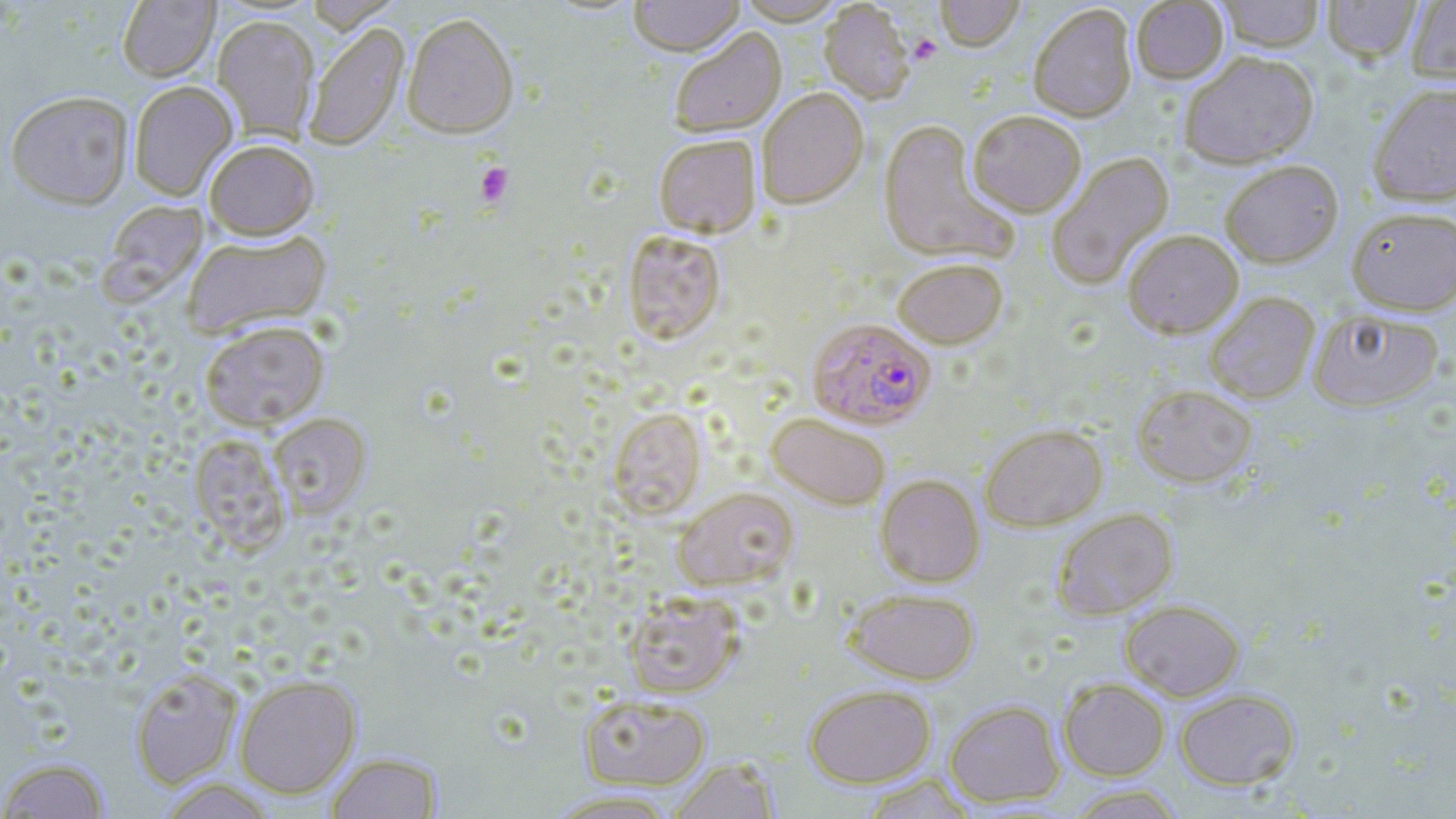 Approximate bounding boxes as [x1, y1, x2, y2] in pixels. Uninfected red blood cell locations: [303, 0, 401, 32], [629, 0, 744, 56], [736, 0, 847, 24], [936, 0, 1024, 51], [1215, 0, 1326, 51], [1322, 0, 1422, 64], [1406, 0, 1456, 84], [117, 1, 219, 82], [818, 1, 915, 103], [1131, 1, 1228, 83], [1028, 3, 1138, 122], [402, 12, 519, 139], [212, 14, 320, 141], [303, 21, 410, 152], [668, 27, 786, 137], [1179, 50, 1318, 168], [128, 80, 238, 201], [1368, 81, 1456, 206], [756, 87, 869, 208], [6, 89, 133, 209], [968, 110, 1086, 216], [877, 121, 1016, 265], [653, 134, 761, 238], [204, 139, 320, 239], [1046, 151, 1174, 290], [1219, 159, 1344, 268], [97, 200, 208, 305], [1345, 205, 1456, 315], [621, 229, 726, 345], [1122, 229, 1244, 337], [182, 230, 333, 338], [892, 257, 1008, 348], [1204, 292, 1320, 404], [1307, 307, 1445, 412], [199, 320, 330, 430], [1132, 384, 1258, 488], [607, 407, 706, 520], [765, 411, 892, 510], [267, 413, 371, 519], [980, 423, 1108, 530], [189, 434, 291, 553], [875, 474, 985, 587], [672, 486, 798, 590], [1050, 507, 1178, 620], [846, 587, 979, 685], [622, 590, 745, 698], [1119, 598, 1245, 701], [130, 668, 242, 789], [234, 674, 361, 798], [1058, 677, 1170, 781], [804, 683, 936, 788], [1174, 688, 1300, 790], [579, 693, 711, 790], [944, 699, 1065, 807], [324, 752, 444, 818], [0, 757, 112, 818], [668, 758, 781, 818], [860, 774, 978, 818], [155, 778, 279, 819], [1064, 784, 1187, 818], [542, 789, 682, 818]. Plasmodium falciparum-infected red blood cell locations: [807, 317, 936, 429]. Platelet locations: [908, 35, 941, 65], [475, 163, 514, 207]. Slide-level diagnosis: Plasmodium falciparum. One field of a larger specimen. Image is 1456×819 pixels. 1000x magnification. Thin blood film. May-Grünwald-Giemsa stain. Optical microscopy.